Identify the blood parasite species.
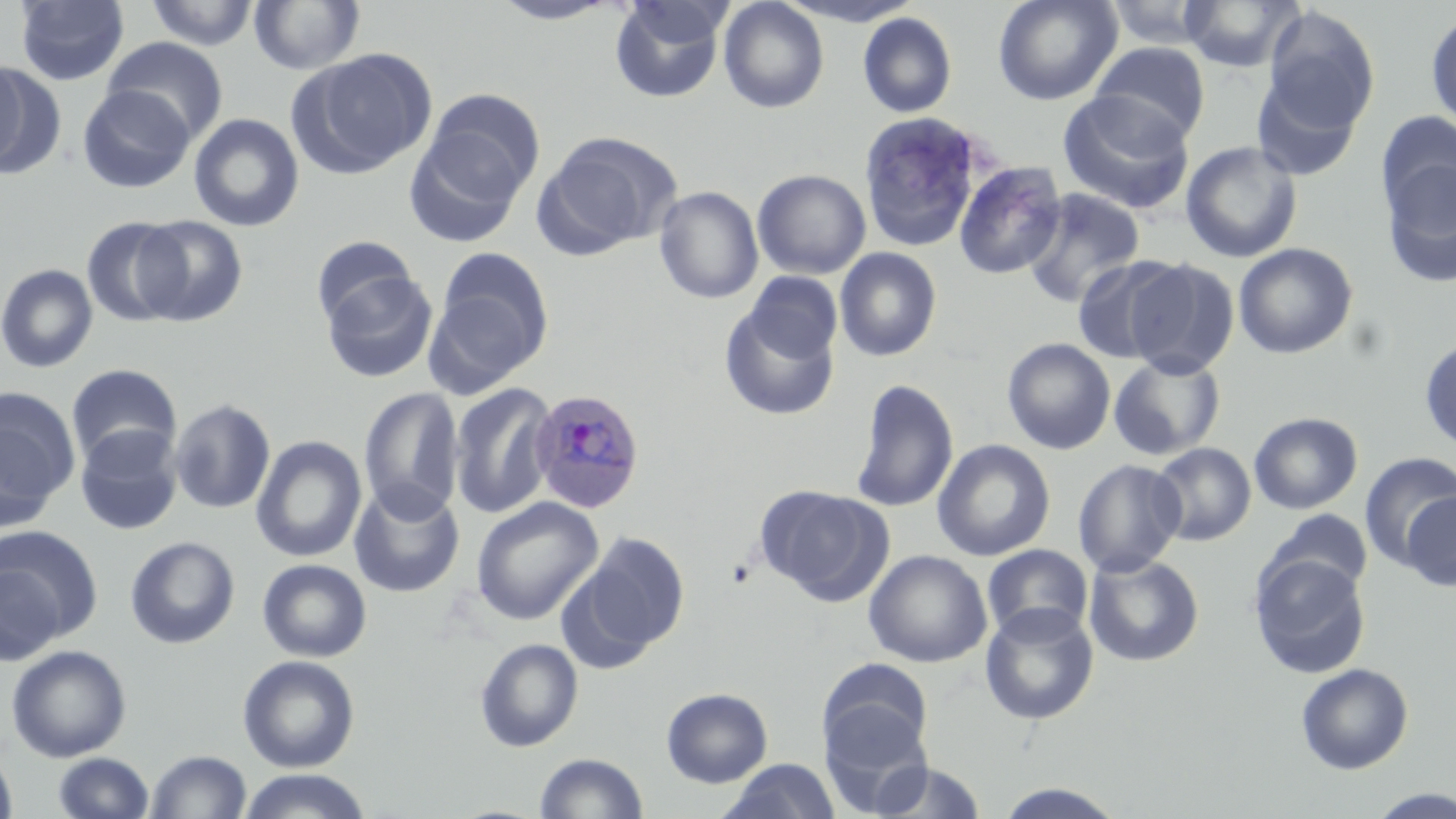
Plasmodium ovale.

Summary:
  - Coordinate format: approximate bounding boxes as [x1, y1, x2, y2] in pixels
  - Plasmodium ovale-infected red blood cell locations: [529, 389, 646, 515]
  - Uninfected red blood cell locations: [15, 0, 129, 86], [718, 0, 829, 113], [993, 0, 1122, 105], [1177, 0, 1305, 72], [144, 1, 260, 50], [249, 1, 365, 75], [488, 1, 621, 26], [608, 1, 728, 104], [772, 1, 922, 27], [1101, 1, 1220, 49], [1263, 7, 1380, 130], [858, 12, 957, 118], [1426, 12, 1456, 131], [102, 37, 227, 143], [1090, 43, 1210, 145], [297, 49, 436, 176], [0, 57, 39, 176], [1252, 71, 1364, 182], [77, 85, 195, 193], [418, 88, 545, 215], [1057, 91, 1195, 214], [858, 111, 988, 250], [1376, 111, 1456, 231], [188, 113, 305, 232], [538, 131, 682, 255], [1180, 141, 1303, 263], [1380, 152, 1456, 288], [954, 161, 1067, 279], [753, 169, 871, 279], [653, 186, 764, 304], [1021, 188, 1145, 308], [132, 215, 248, 327], [81, 216, 190, 328], [311, 236, 419, 329], [1233, 242, 1358, 359], [834, 248, 942, 362], [429, 252, 553, 386], [1070, 254, 1186, 363], [1124, 259, 1240, 379], [0, 263, 98, 374], [321, 270, 438, 383], [743, 272, 843, 365], [718, 300, 838, 423], [1419, 336, 1456, 454], [1002, 337, 1116, 455], [1108, 353, 1226, 461], [66, 364, 182, 470], [849, 379, 959, 513], [448, 381, 557, 521], [358, 386, 464, 523], [0, 387, 81, 527], [169, 399, 276, 514], [1248, 412, 1363, 515], [75, 426, 183, 535], [251, 436, 366, 562], [932, 439, 1055, 561], [1150, 442, 1256, 546], [1359, 452, 1456, 570], [1073, 458, 1186, 578], [349, 481, 465, 598], [754, 484, 889, 603], [1402, 491, 1456, 592], [470, 497, 604, 625], [1260, 509, 1373, 601], [0, 525, 103, 651], [574, 532, 690, 661], [125, 536, 240, 649], [982, 544, 1093, 643], [863, 550, 992, 668], [1083, 554, 1205, 667], [1249, 554, 1372, 679], [257, 559, 372, 662], [0, 561, 66, 667], [980, 604, 1099, 725], [475, 638, 583, 752], [5, 644, 132, 762], [237, 654, 360, 773], [817, 659, 934, 766], [1295, 663, 1414, 775], [661, 687, 773, 788], [819, 707, 933, 816], [0, 747, 18, 819], [146, 749, 251, 818], [52, 752, 154, 818], [534, 752, 648, 819], [720, 758, 842, 819], [867, 759, 988, 819], [238, 769, 372, 819], [991, 782, 1130, 817], [1366, 788, 1456, 818]
  - Stain: May-Grünwald-Giemsa
  - Magnification: 1000x
  - Field of view: single
  - Modality: optical microscopy
  - Preparation: thin blood smear
  - Image size: 1456×819 pixels